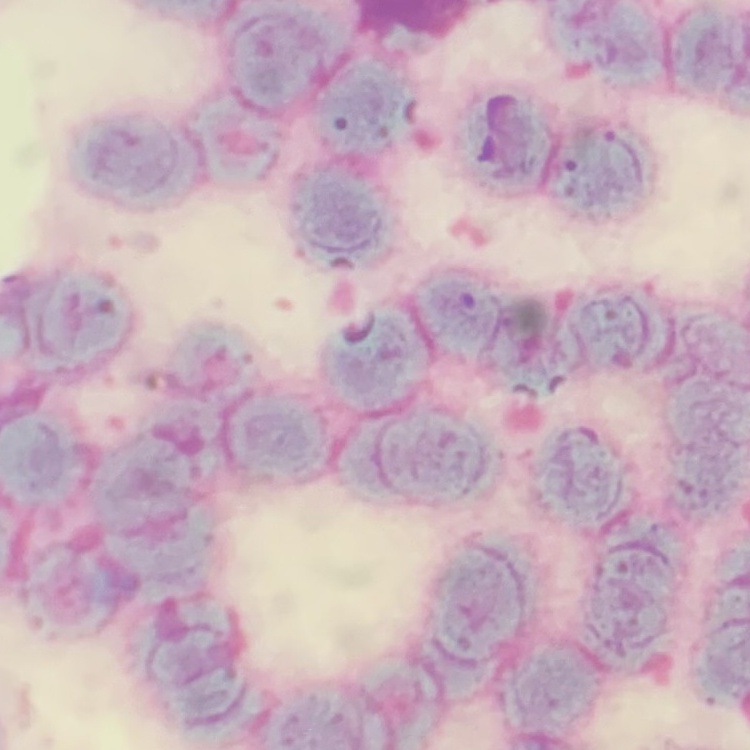
red blood cell morphology = rouleaux formation
preparation = thin blood smear
stain = Field's or Giemsa
image type = one tile cut from a larger photomicrograph